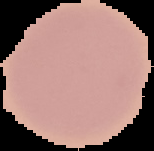
preparation = thin blood film
image size = 154×151 pixels
image type = segmented cell region on a black background
malaria status = uninfected